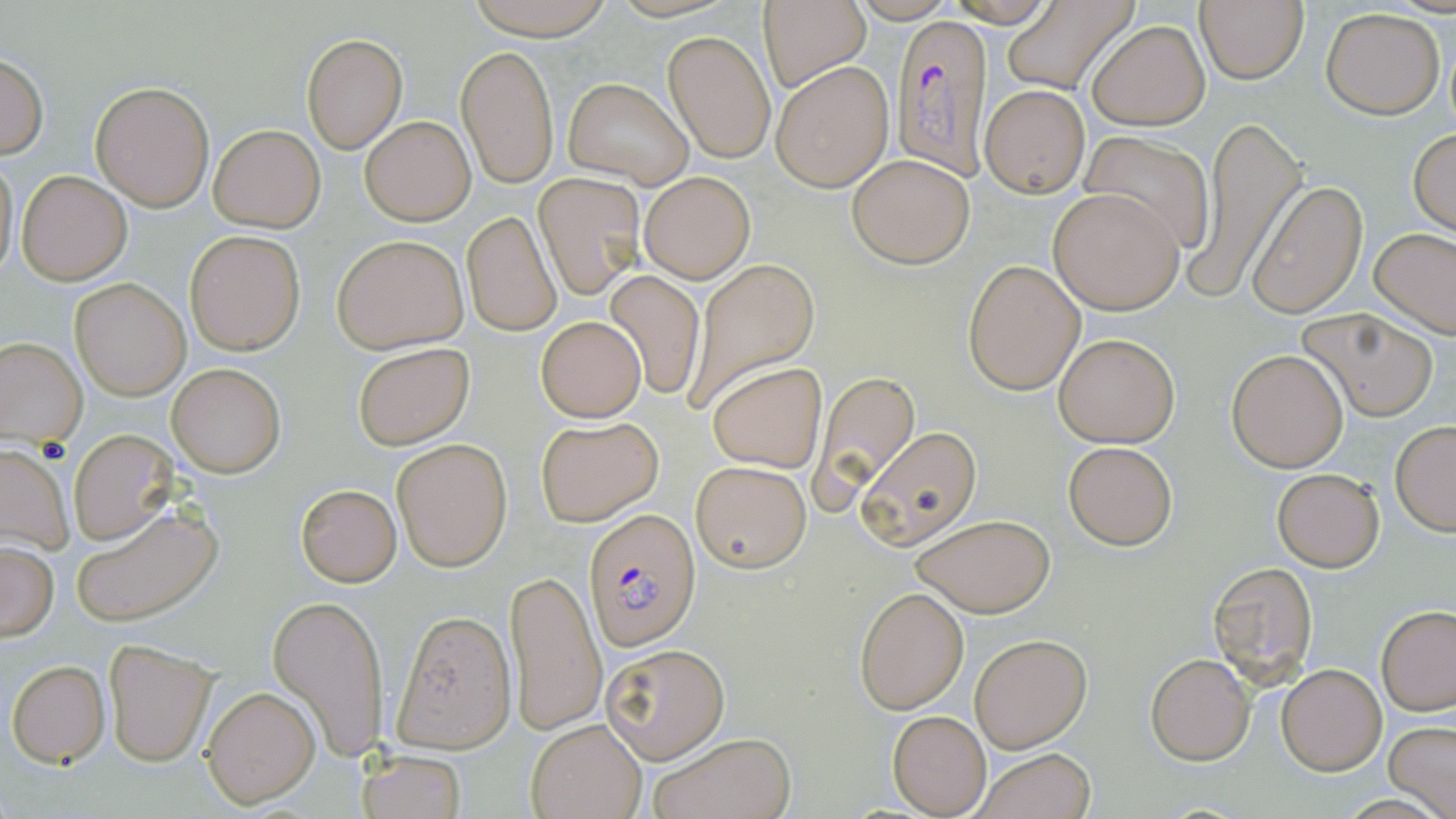
Approximate bounding boxes as [x1, y1, x2, y2] in pixels. Plasmodium falciparum-infected red blood cell locations: [891, 13, 997, 181], [583, 507, 698, 649]. Uninfected red blood cell locations: [460, 0, 619, 39], [759, 1, 869, 93], [1195, 2, 1309, 84], [1000, 4, 1135, 92], [1321, 7, 1445, 119], [1088, 20, 1209, 129], [663, 31, 776, 163], [302, 34, 407, 153], [456, 44, 559, 186], [0, 53, 48, 159], [770, 60, 894, 193], [563, 77, 692, 189], [90, 80, 216, 213], [979, 84, 1089, 197], [360, 114, 475, 225], [1187, 115, 1307, 304], [209, 124, 325, 232], [1408, 128, 1456, 236], [1082, 130, 1217, 254], [1, 152, 20, 280], [848, 154, 974, 269], [17, 171, 131, 285], [639, 171, 753, 283], [533, 172, 644, 300], [1246, 181, 1368, 318], [1048, 186, 1186, 314], [461, 210, 561, 337], [1370, 225, 1456, 339], [185, 229, 305, 356], [332, 234, 468, 354], [683, 257, 821, 416], [964, 259, 1086, 397], [604, 270, 706, 399], [70, 278, 190, 400], [1301, 308, 1438, 420], [535, 316, 645, 422], [1052, 332, 1180, 448], [0, 335, 88, 445], [352, 341, 473, 450], [1226, 348, 1348, 472], [165, 360, 287, 478], [706, 361, 827, 474], [817, 371, 920, 501], [536, 415, 664, 529], [1390, 421, 1456, 536], [859, 427, 981, 552], [68, 430, 180, 545], [393, 438, 512, 571], [1063, 441, 1177, 550], [0, 445, 73, 553], [691, 461, 812, 571], [1271, 468, 1384, 571], [296, 484, 401, 587], [71, 503, 223, 627], [910, 514, 1056, 618], [0, 540, 59, 641], [1207, 561, 1319, 685], [506, 569, 606, 734], [855, 587, 969, 714], [268, 591, 390, 761], [1377, 605, 1455, 715], [391, 610, 516, 754], [971, 633, 1090, 752], [103, 639, 217, 767], [599, 641, 731, 764], [1145, 653, 1256, 766], [7, 659, 110, 767], [1277, 663, 1386, 776], [200, 684, 321, 809], [887, 710, 992, 816], [526, 718, 647, 818], [1385, 721, 1456, 817], [646, 732, 794, 819], [359, 748, 467, 819], [971, 749, 1095, 819]. Slide-level diagnosis: Plasmodium falciparum. Image is 1456×819 pixels. May-Grünwald-Giemsa-stained preparation. Thin blood film. Single field of view. Captured at 1000x magnification. Light microscopy.